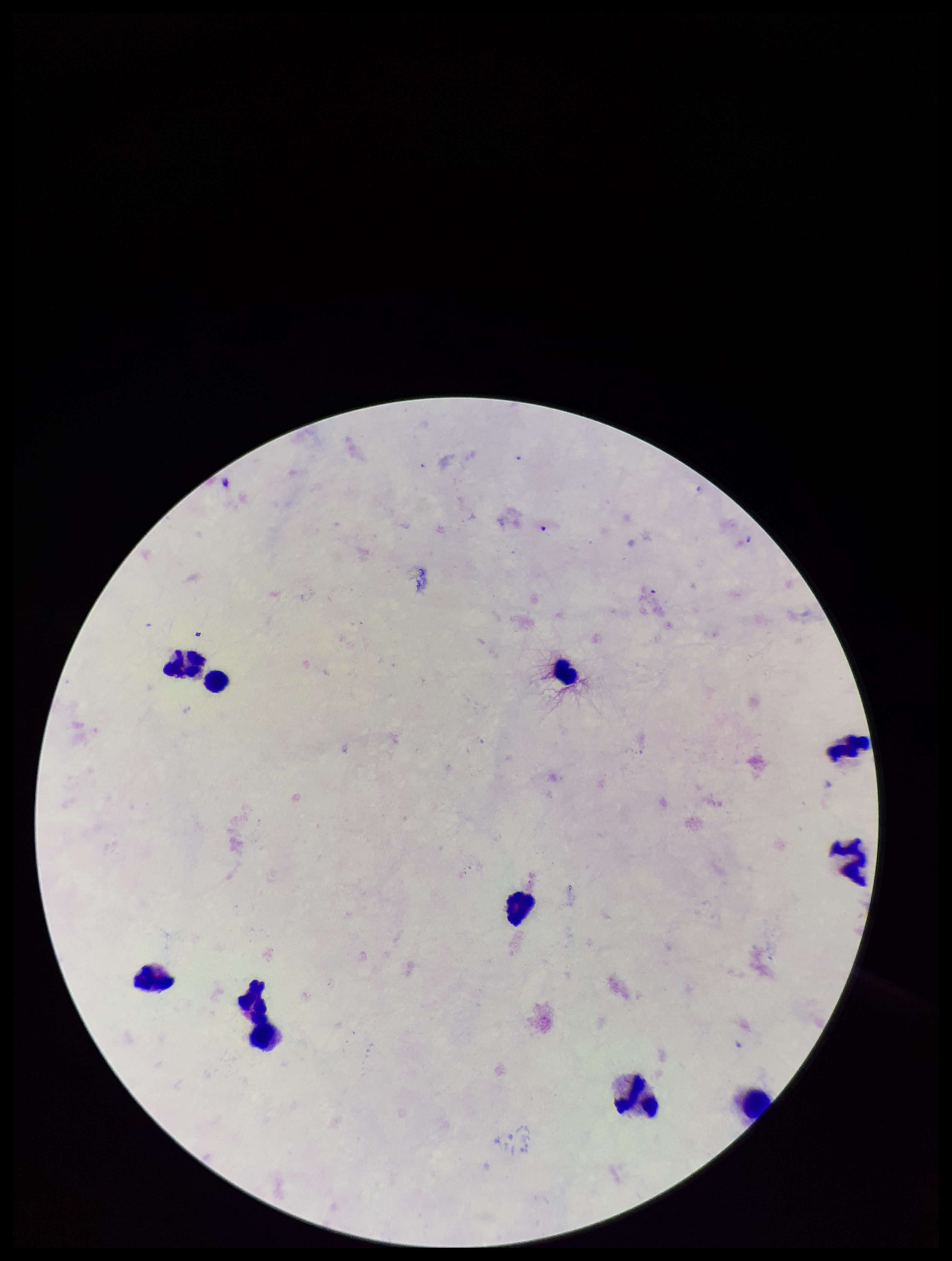
Summary:
  - Field of view: single
  - Species reported for this patient: Plasmodium falciparum
  - Preparation: thick smear
  - Image size: 952×1261 pixels
  - Stain: Giemsa
  - Leukocyte count: 10
  - Capture: smartphone photograph through the microscope eyepiece
  - Parasite count: 0
  - Patient malaria status: infected
  - Plasmodium parasites: none seen